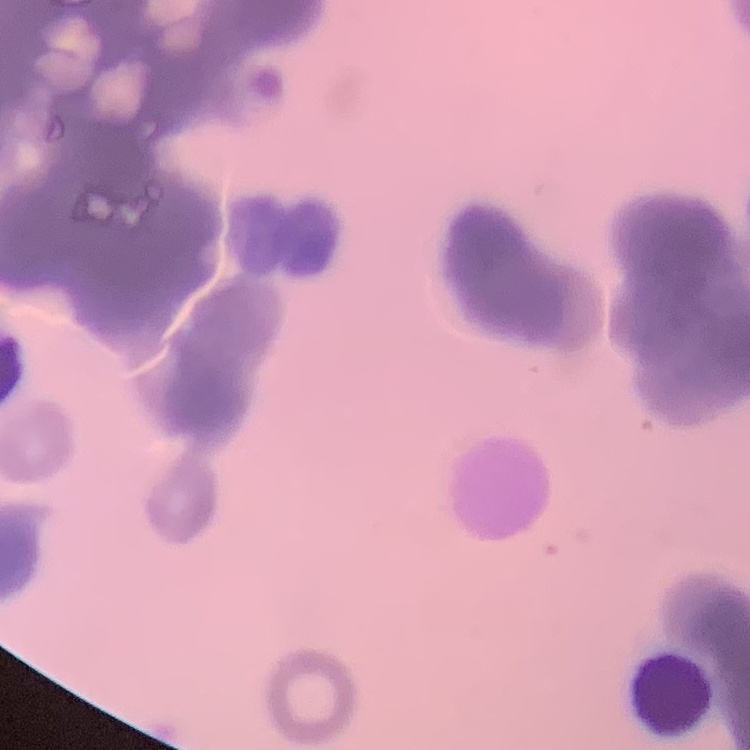

Summary:
  - Red blood cell morphology: rouleaux formation
  - Image type: square crop of a larger photomicrograph
  - Stain: Field's or Giemsa
  - Preparation: thin blood film